Assess this cell for malaria.
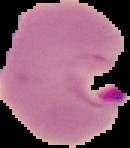

Parasitized.

{
  "image_type": "cell region segmented out of the field of view; surrounding area masked to black",
  "preparation": "thin blood film",
  "image_size": "130×148 pixels"
}